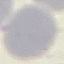

Summary:
  - Malaria status: uninfected
  - Preparation: thin smear
  - Image type: cell patch, automatically extracted from a larger field of view and resized to 64 × 64 pixels
  - Stain: Giemsa
  - Capture: smartphone through the microscope eyepiece